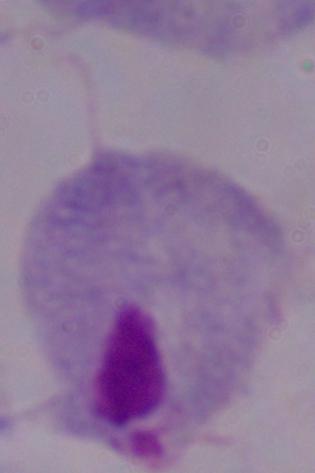

identification = trichomonad
magnification = 1000x
modality = micrograph